Identify the parasite.
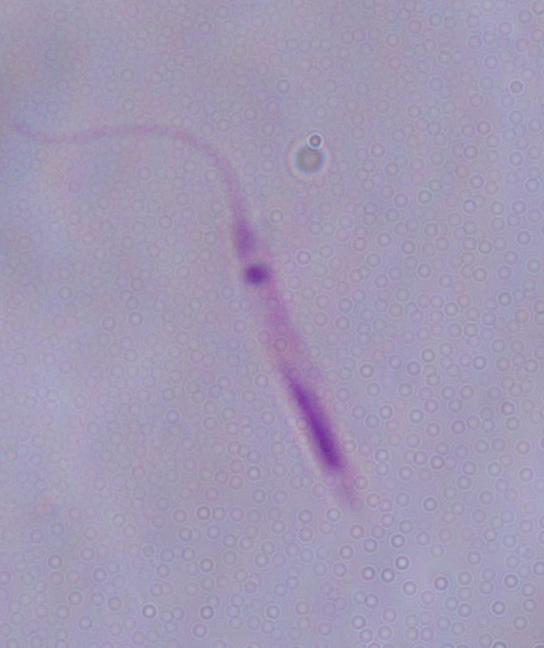
Leishmania.

modality = micrograph
magnification = 1000x